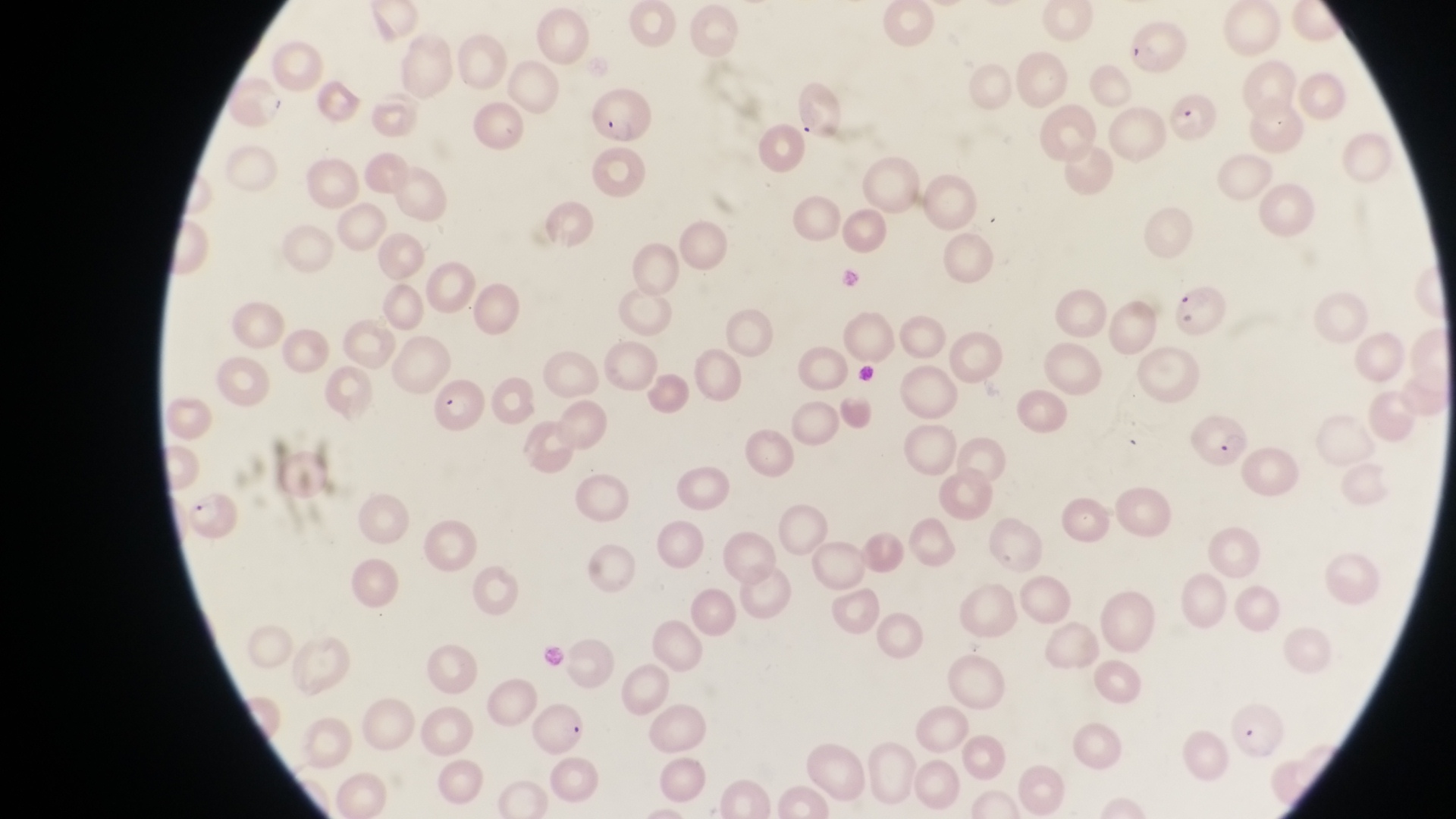

Approximate bounding boxes as {left, top, right, bottom} in pixels. Parasitised red blood cell locations: {1122, 14, 1181, 70}, {592, 93, 651, 142}, {1166, 96, 1222, 145}, {1176, 285, 1228, 341}, {433, 378, 502, 437}, {1188, 415, 1248, 464}. Image is 1456×819 pixels. Single field of view. Captured by a smartphone held over the eyepiece of an Olympus CX-23 microscope. Collected in Uganda. Thin blood smear. At a magnification of 1000x.